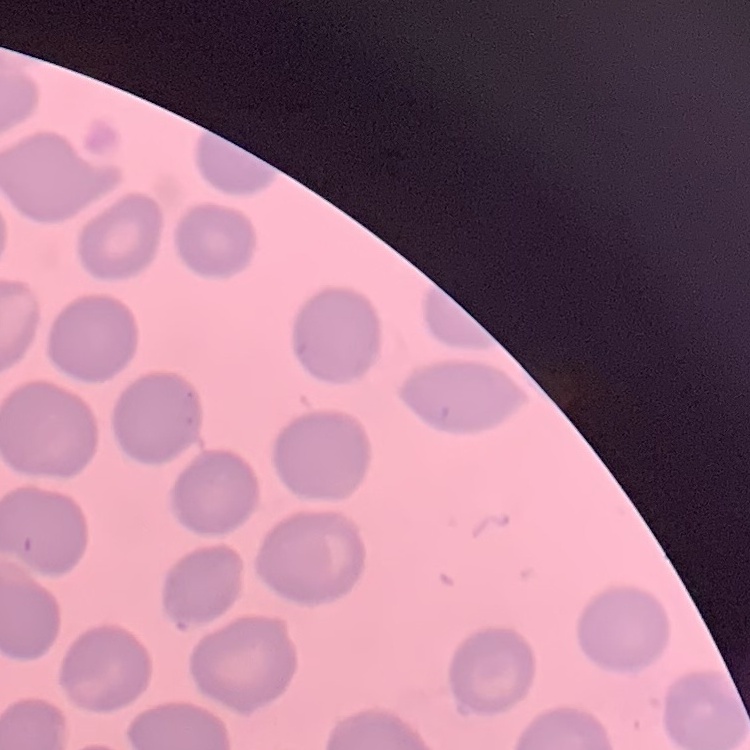
Summary:
  - Erythrocyte morphology: no rouleaux formation
  - Image type: square crop of a larger photomicrograph
  - Stain: Field's or Giemsa
  - Preparation: thin blood film